Describe the morphology of the erythrocytes.
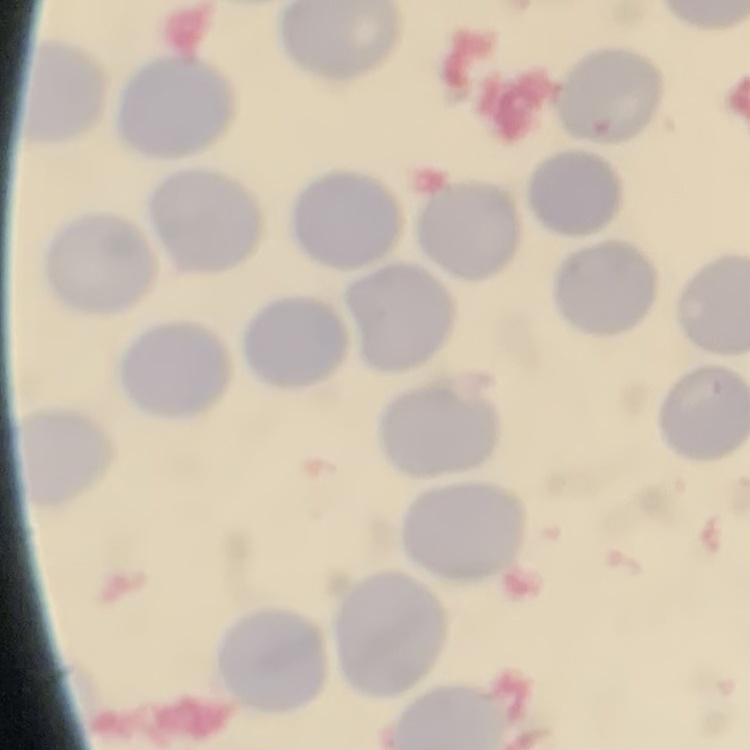

They show no rouleaux formation.

stain: Field's or Giemsa
image_type: one tile cut from a larger photomicrograph
preparation: thin peripheral smear